Identify the parasite.
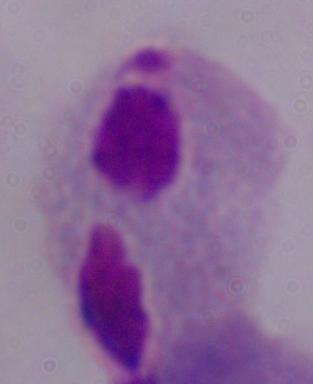
This is a trichomonad.

Summary:
  - Magnification: 1000x
  - Modality: photomicrograph